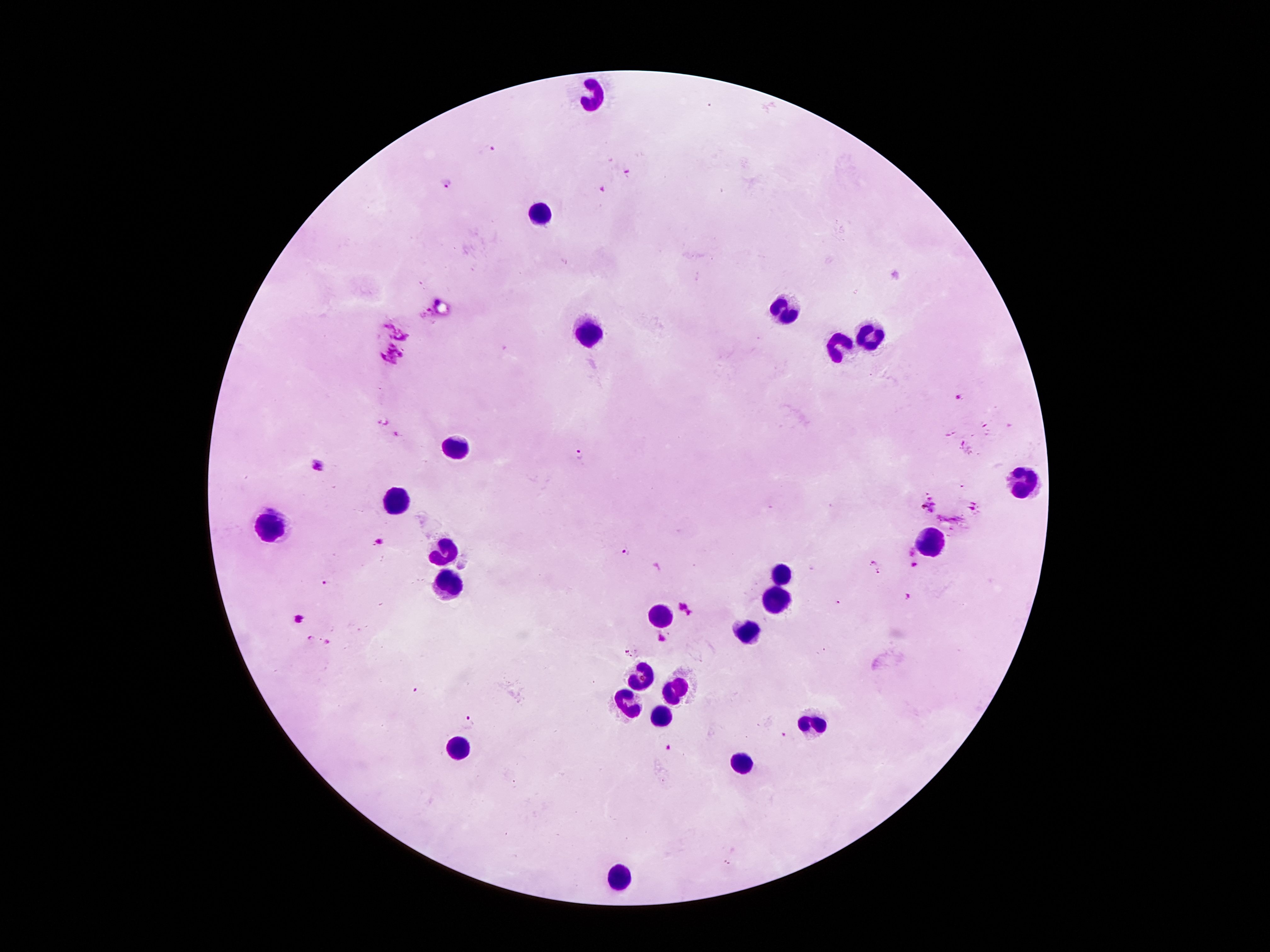
coordinate format = approximate centers as (x, y) in pixels
leukocyte locations = (591, 90), (542, 212), (782, 311), (588, 332), (866, 332), (838, 347), (458, 446), (1021, 479), (397, 495), (265, 517), (929, 545), (446, 548), (782, 571), (453, 579), (784, 604), (657, 612), (746, 629), (649, 673), (672, 685), (626, 701), (660, 713), (815, 724), (458, 747), (738, 762), (621, 876)
malaria parasite locations = (491, 151), (627, 173), (446, 185), (605, 188), (958, 396), (580, 454), (317, 463), (928, 506), (378, 541), (626, 552), (914, 565), (326, 583), (909, 598), (687, 607), (300, 618), (310, 635), (663, 639), (329, 642), (629, 652), (415, 691), (470, 721), (784, 734), (670, 748)
image size = 1270×952 pixels
field of view = single
stain = Giemsa
capture = smartphone camera through the microscope eyepiece
magnification = 100x
preparation = thick peripheral-blood smear
patient malaria status = positive for Plasmodium falciparum